Classify this cell by malaria status.
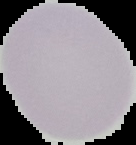
It is uninfected.

image_type: segmented cell region with the area outside set to black
image_size: 136×145 pixels
preparation: thin blood film